Report the malaria status of this cell.
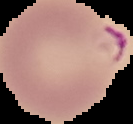

It is parasitized.

image type = cell region segmented out of the field of view; surrounding area masked to black
preparation = thin blood smear
image size = 133×124 pixels